Mark where platelets are.
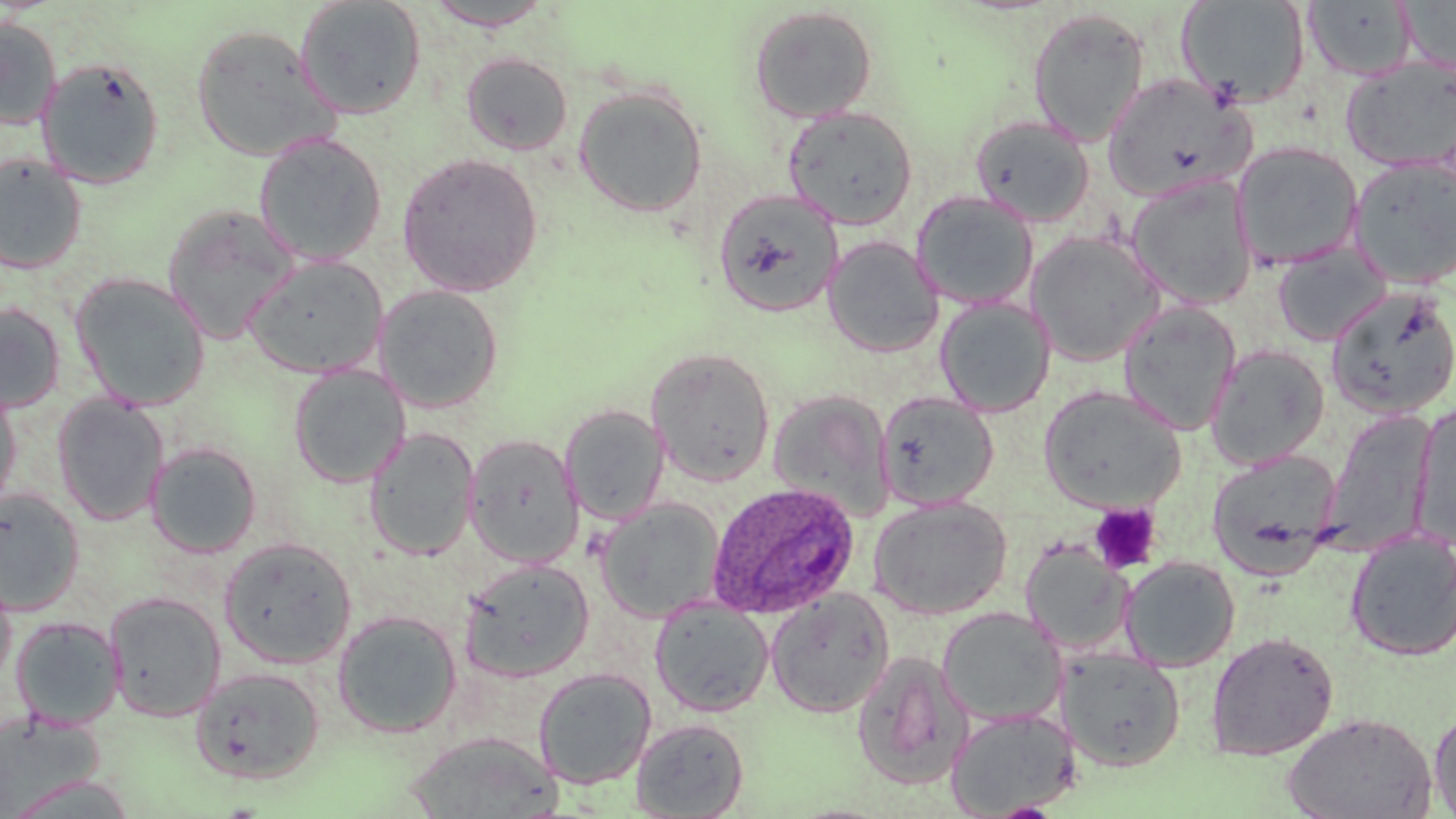

Approximate bounding boxes as (x1, y1, x2, y2) in pixels.
Platelets: (1090, 503, 1161, 574).

{
  "slide_level_diagnosis": "Plasmodium ovale",
  "uninfected_red_blood_cell_locations": "approximate bounding boxes as (x1, y1, x2, y2) in pixels: (293, 0, 426, 119), (423, 1, 555, 31), (1177, 1, 1311, 109), (1304, 1, 1418, 81), (1401, 1, 1456, 76), (749, 5, 878, 124), (1027, 7, 1150, 146), (0, 17, 62, 129), (191, 24, 339, 162), (461, 52, 574, 156), (1341, 56, 1456, 173), (37, 57, 165, 189), (1101, 72, 1256, 202), (573, 85, 707, 217), (783, 105, 918, 228), (969, 115, 1095, 227), (253, 131, 387, 266), (1231, 141, 1364, 270), (397, 152, 543, 296), (0, 153, 88, 273), (1347, 156, 1456, 290), (1124, 174, 1258, 310), (713, 189, 843, 318), (911, 190, 1039, 311), (161, 203, 301, 344), (1026, 230, 1165, 366), (823, 235, 943, 358), (1272, 243, 1392, 347), (244, 254, 389, 379), (70, 272, 211, 411), (373, 284, 505, 413), (1325, 286, 1455, 419), (934, 297, 1055, 417), (1118, 300, 1242, 436), (0, 302, 66, 414), (1206, 344, 1330, 470), (646, 346, 776, 487), (288, 363, 411, 488), (0, 382, 23, 517), (1038, 384, 1185, 513), (767, 389, 896, 523), (876, 391, 999, 510), (52, 394, 170, 526), (1411, 401, 1456, 549), (560, 404, 670, 525), (1320, 410, 1438, 556), (365, 427, 480, 561), (464, 433, 584, 568), (146, 442, 262, 558), (1207, 449, 1342, 578), (0, 488, 85, 616), (869, 496, 1012, 619), (596, 499, 725, 621), (1346, 529, 1456, 661), (219, 537, 356, 668), (1020, 539, 1133, 656), (1120, 555, 1240, 672), (460, 558, 594, 683), (0, 570, 16, 689), (765, 587, 895, 718), (104, 591, 227, 722), (649, 599, 775, 718), (937, 607, 1067, 727), (331, 609, 463, 738), (11, 616, 125, 730), (1205, 631, 1339, 760), (1057, 647, 1185, 771), (851, 650, 973, 791), (190, 665, 325, 785), (532, 667, 657, 789), (944, 707, 1082, 818), (1429, 707, 1456, 816), (0, 710, 109, 813), (1282, 711, 1437, 819), (630, 717, 749, 818), (404, 731, 563, 819)",
  "image_size": "1456×819 pixels",
  "plasmodium_ovale_infected_red_blood_cell_locations": "approximate bounding boxes as (x1, y1, x2, y2) in pixels: (706, 481, 860, 618)",
  "field_of_view": "one of a larger specimen",
  "magnification": "1000x",
  "preparation": "thin blood film",
  "modality": "optical microscopy",
  "stain": "May-Grünwald-Giemsa"
}